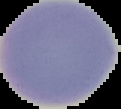
malaria_status: uninfected
image_size: 121×109 pixels
preparation: thin blood smear
image_type: segmented cell region on a black background